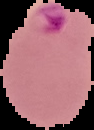

Image is 94×130 pixels. Result: malaria parasites detected. Segmented cell region on a black background. From a thin blood film.